Locate every P. falciparum parasite and give its life-cycle stage, and locate every leukocyte and any debris.
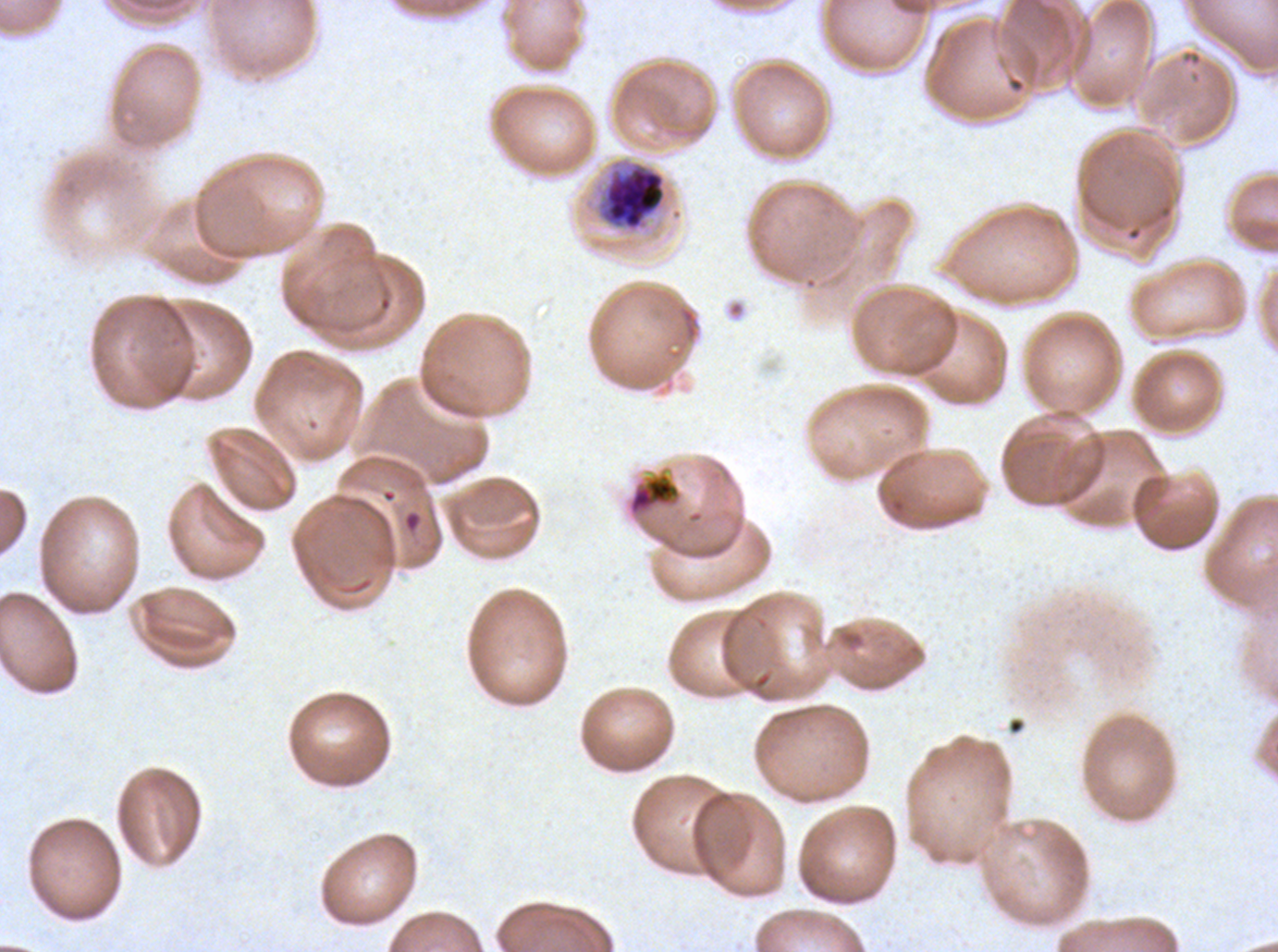
Approximate bounding boxes as (x1, y1, x2, y2) in pixels.
Early schizonts: (596, 162, 667, 232).
Debris: (626, 470, 683, 520).
No rings, late-ring/early-trophozoite forms, mid trophozoites, late trophozoites, late schizonts, segmenters, gametocytes, or leukocytes observed.

P. falciparum cultured ex vivo for 24 to 48 hours, from a patient in The Gambia. Image is 1278×952 pixels. One sub-image of a larger composite. Thin blood film. Giemsa-stained preparation.